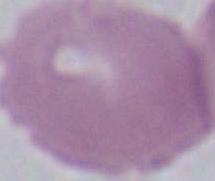 Micrograph. 1000x magnification. A red blood cell is shown.